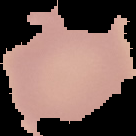
Segmented cell region on a black background. Malaria status: uninfected. From a thin blood film. Image is 136×136 pixels.